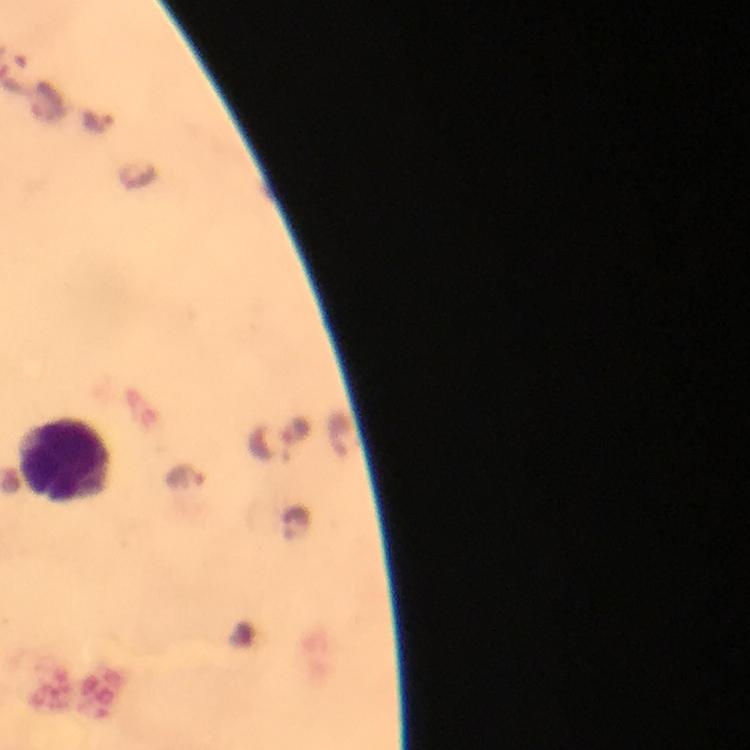

Approximate object centers, in pixels from the top-left corner.
Summary:
  - Plasmodium parasite locations: (x=96, y=122), (x=268, y=442), (x=186, y=477)
  - Leukocyte locations: (x=62, y=459)
  - Stain: Giemsa
  - Magnification: 100x
  - Context: from a diagnostic examination for malaria
  - Immersion oil: applied
  - Capture: smartphone photograph through a microscope
  - Cropped from: a single field of view
  - Image size: 750×750 pixels
  - Preparation: thick blood film